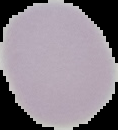 From a thin blood smear. Malaria status: uninfected. The area outside the segmented cell region is set to black. Image is 118×130 pixels.